Locate every blood parasite and identify its species.
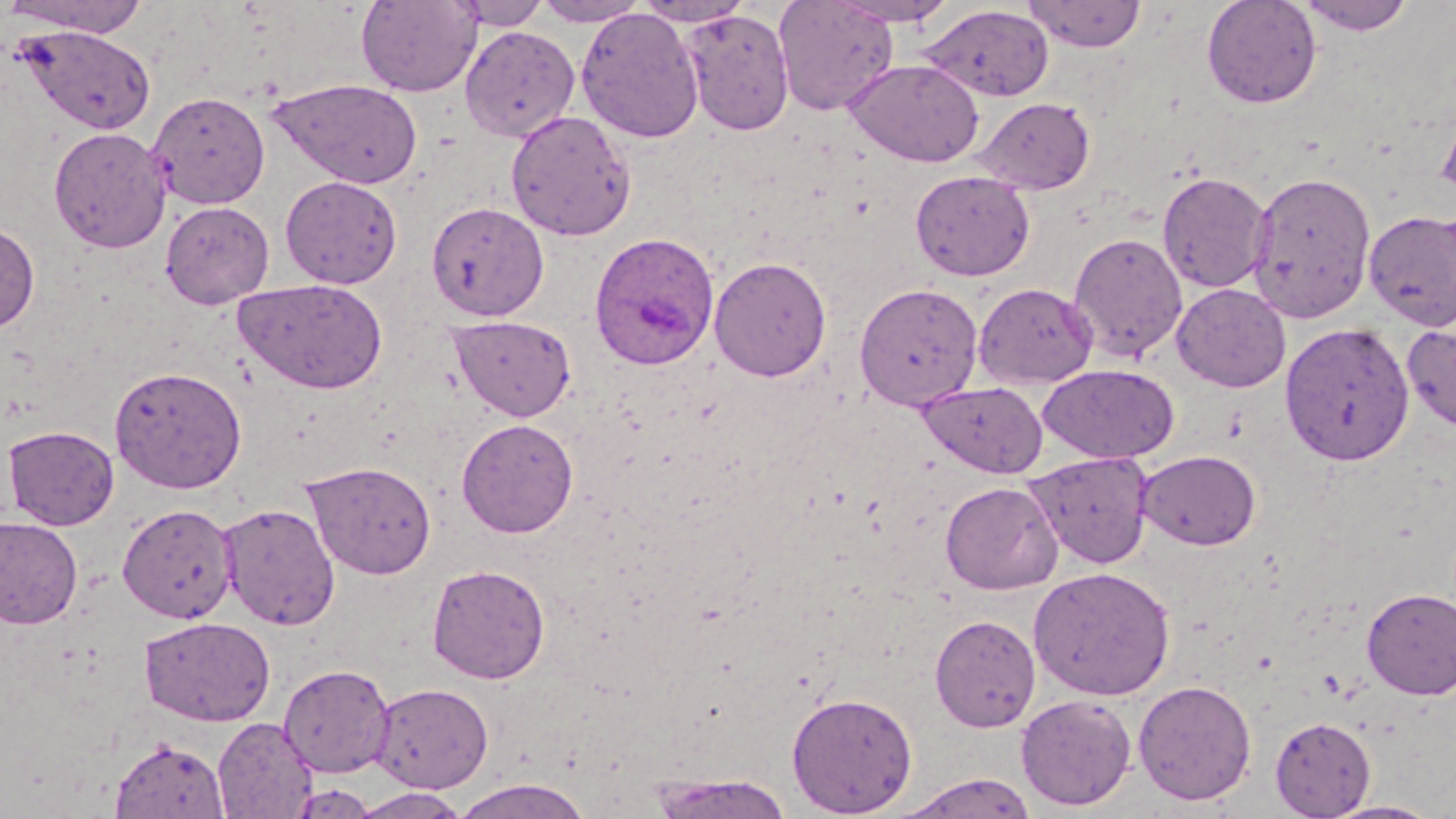

Approximate bounding boxes as (x1, y1, x2, y2) in pixels.
Plasmodium ovale-infected red blood cells: (588, 232, 719, 371).
No Plasmodium falciparum, Plasmodium malariae, Plasmodium vivax, Babesia divergens, or Trypanosoma brucei observed.

slide-level diagnosis = Plasmodium ovale
magnification = 1000x
image size = 1456×819 pixels
preparation = thin blood smear
stain = May-Grünwald-Giemsa
uninfected red blood cell locations = approximate bounding boxes as (x1, y1, x2, y2) in pixels: (1, 0, 152, 37), (356, 0, 482, 97), (452, 0, 551, 29), (634, 0, 753, 27), (773, 0, 899, 116), (830, 0, 960, 26), (1022, 0, 1147, 52), (1201, 0, 1323, 109), (1296, 0, 1417, 35), (533, 1, 648, 26), (921, 5, 1054, 102), (576, 8, 705, 144), (681, 9, 795, 136), (14, 25, 156, 134), (460, 26, 580, 141), (844, 59, 985, 167), (268, 78, 423, 189), (148, 91, 270, 210), (974, 97, 1096, 195), (1436, 103, 1456, 206), (505, 110, 637, 241), (48, 127, 171, 252), (910, 170, 1036, 281), (1247, 170, 1377, 324), (1157, 171, 1272, 293), (280, 176, 402, 289), (1270, 196, 1456, 330), (160, 201, 274, 308), (426, 201, 549, 321), (1363, 210, 1456, 332), (0, 221, 40, 333), (1068, 232, 1187, 363), (709, 256, 832, 381), (235, 278, 387, 394), (854, 282, 984, 410), (973, 282, 1098, 389), (1171, 283, 1291, 393), (448, 315, 577, 421), (1279, 321, 1415, 467), (1402, 321, 1456, 433), (1039, 364, 1179, 464), (110, 365, 247, 494), (916, 381, 1048, 477), (456, 418, 578, 538), (3, 425, 119, 529), (1137, 450, 1261, 551), (1025, 451, 1154, 568), (303, 460, 437, 579), (940, 481, 1064, 595), (219, 502, 340, 631), (117, 503, 237, 623), (0, 517, 83, 630), (427, 563, 550, 684), (1028, 566, 1176, 701), (1361, 587, 1456, 699), (930, 613, 1041, 732), (138, 616, 275, 726), (279, 663, 395, 778), (1133, 679, 1257, 805), (369, 683, 494, 793), (787, 691, 918, 816), (1016, 694, 1138, 810), (213, 716, 317, 818), (1270, 717, 1376, 818), (110, 738, 229, 818), (646, 773, 796, 818), (894, 773, 1040, 818), (451, 777, 592, 819), (288, 783, 379, 818), (348, 788, 473, 818), (1320, 799, 1447, 819)
field of view = single
modality = light microscopy